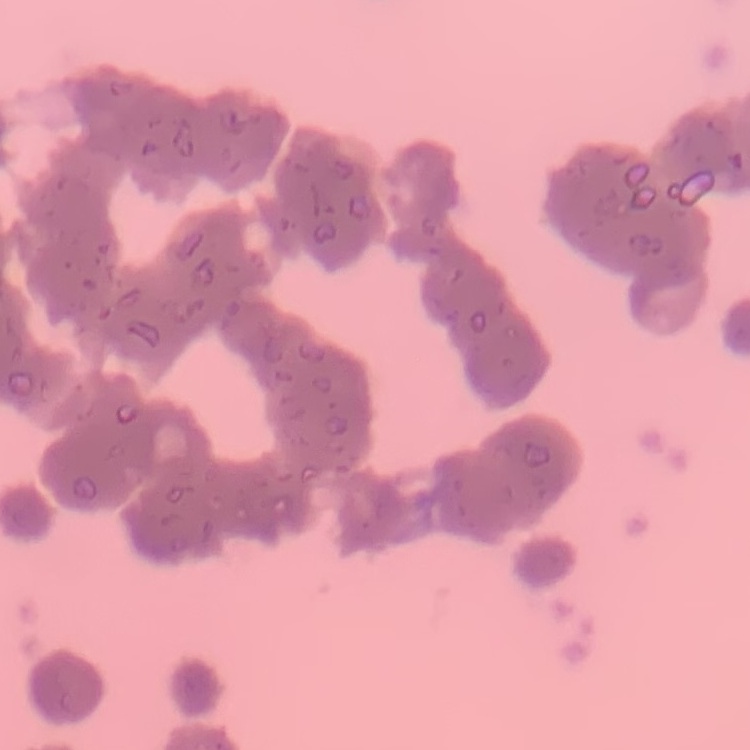
Summary:
  - Red blood cell morphology: rouleaux formation
  - Image type: one tile cut from a larger photomicrograph
  - Preparation: thin peripheral smear
  - Stain: Field's or Giemsa